Report the malaria status of this cell.
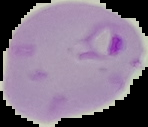
Parasitized.

Cell region segmented out of the field of view; the surrounding area is masked to black. Image is 148×127 pixels. From a thin blood smear.